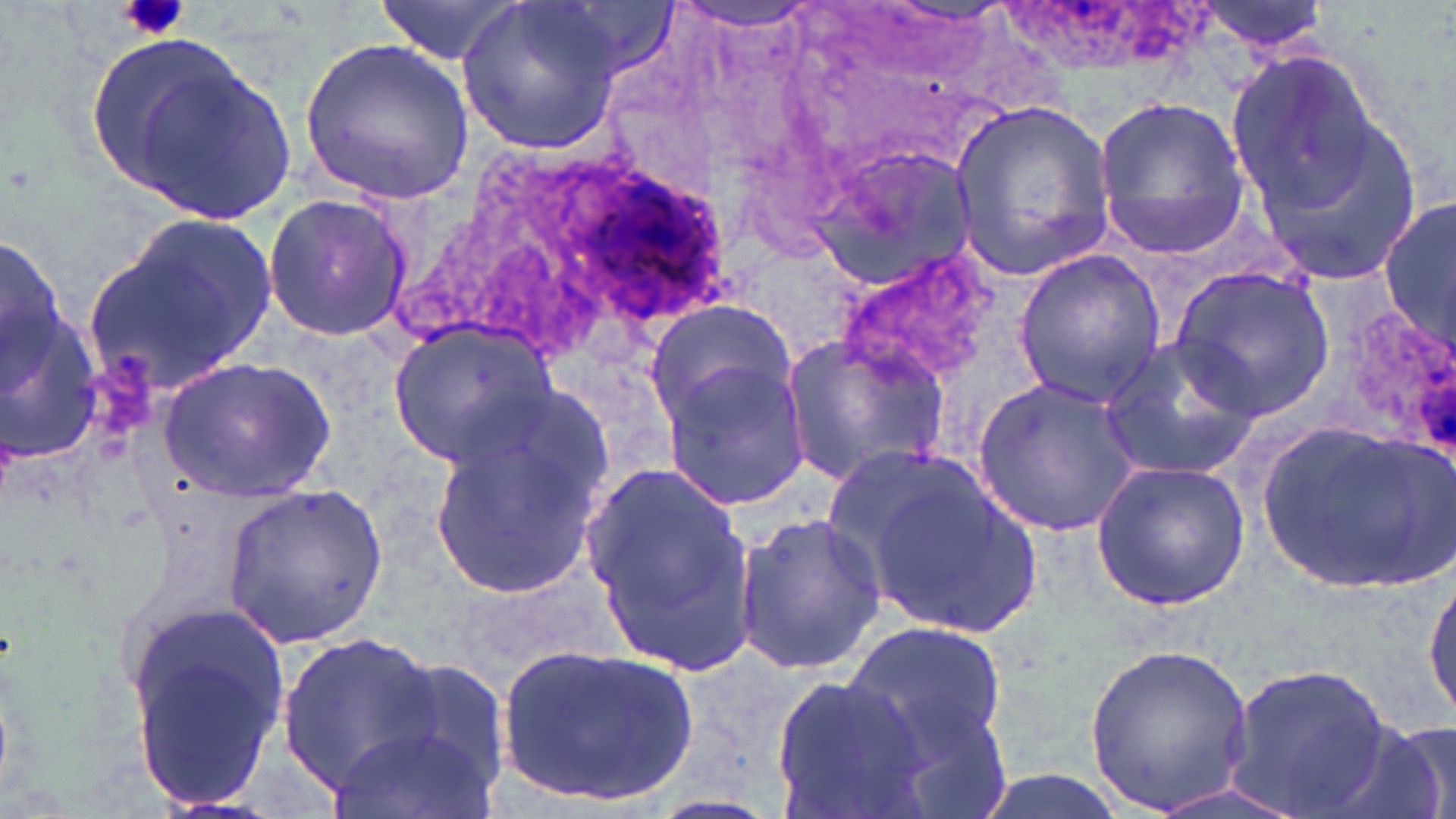
{
  "slide_level_diagnosis": "Plasmodium ovale",
  "modality": "optical microscopy",
  "magnification": "1000x",
  "field_of_view": "single",
  "uninfected_red_blood_cell_locations": "approximate bounding boxes as (x1,y1)-(x2,y2) corner pairs in pixels: (378,0)-(529,64), (456,0)-(625,155), (1195,0)-(1334,56), (665,2)-(823,32), (300,38)-(473,204), (1221,38)-(1389,226), (114,51)-(297,226), (1093,95)-(1250,260), (948,99)-(1115,281), (1246,114)-(1424,282), (813,142)-(977,291), (261,192)-(411,344), (1382,194)-(1456,354), (85,209)-(282,396), (1,222)-(64,405), (1011,248)-(1167,405), (832,249)-(999,387), (1170,265)-(1334,418), (2,291)-(108,478), (644,300)-(798,425), (1330,305)-(1456,459), (389,321)-(557,469), (777,333)-(950,488), (1097,334)-(1261,481), (655,354)-(811,510), (159,356)-(334,502), (974,373)-(1143,540), (428,419)-(606,604), (1259,421)-(1450,593), (581,456)-(757,673), (1090,458)-(1253,611), (850,459)-(1052,642), (222,481)-(391,647), (734,510)-(887,674), (1424,570)-(1456,719), (124,607)-(291,808), (842,618)-(1010,765), (278,630)-(443,788), (1083,641)-(1259,815), (499,642)-(701,811), (383,654)-(514,801), (1224,658)-(1394,815), (770,674)-(927,815), (329,718)-(499,819), (1342,719)-(1456,819), (959,768)-(1134,819), (1135,776)-(1316,819)",
  "platelet_locations": "approximate bounding boxes as (x1,y1)-(x2,y2) corner pairs in pixels: (116,0)-(191,41)",
  "plasmodium_ovale_infected_red_blood_cell_locations": "approximate bounding boxes as (x1,y1)-(x2,y2) corner pairs in pixels: (582,170)-(741,329)",
  "preparation": "thin blood smear",
  "stain": "May-Grünwald-Giemsa",
  "image_size": "1456×819 pixels"
}